Locate and identify every blood parasite.
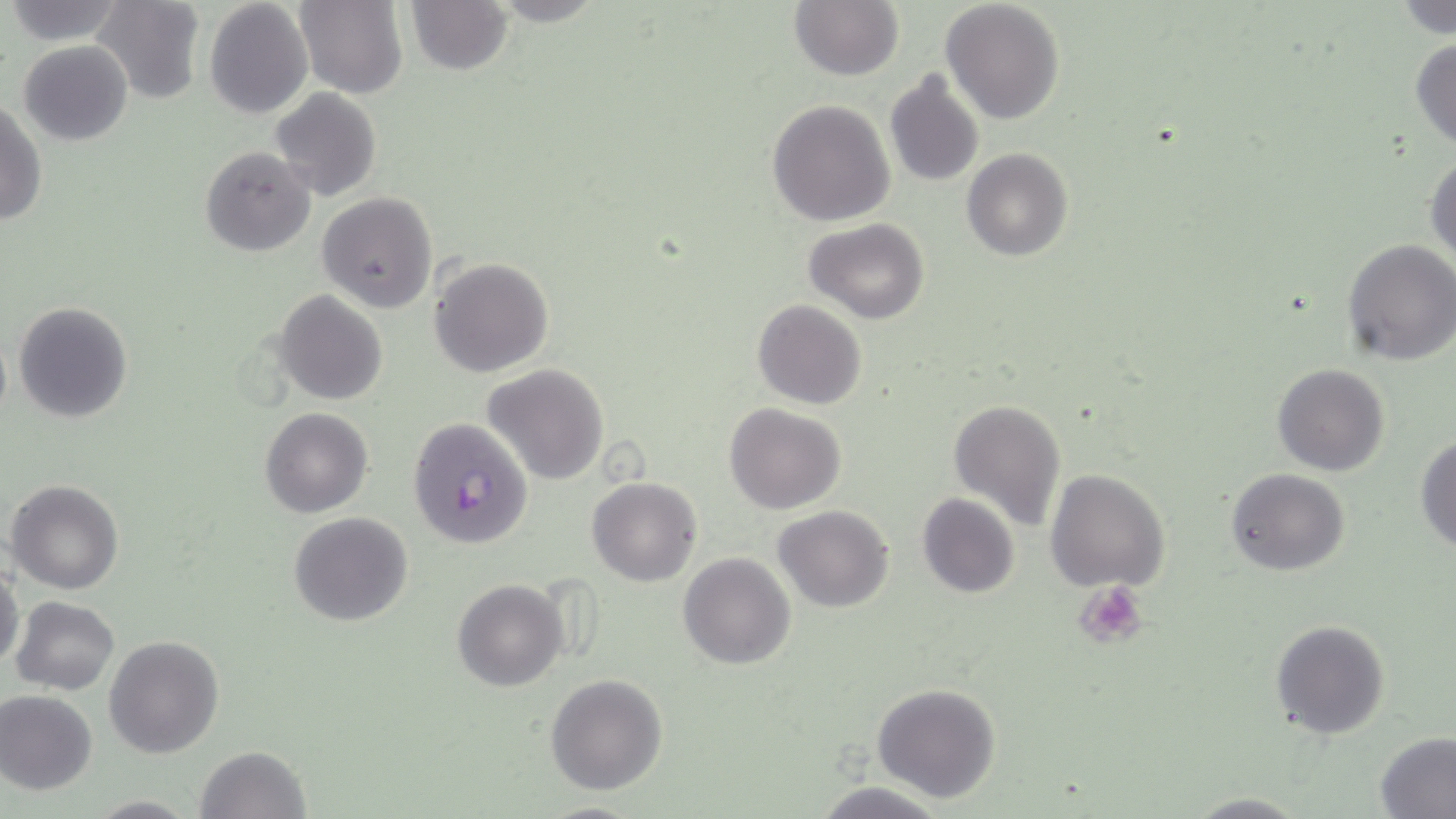
Approximate bounding boxes as named x1/y1/x2/y2 corners in pixels.
Plasmodium falciparum-infected red blood cells: (x1=406, y1=418, x2=533, y2=551).
No Plasmodium ovale, Plasmodium malariae, Plasmodium vivax, Babesia divergens, or Trypanosoma brucei observed.

Summary:
  - Platelet locations: (x1=1072, y1=581, x2=1147, y2=649)
  - Uninfected red blood cell locations: (x1=91, y1=0, x2=206, y2=104), (x1=205, y1=0, x2=313, y2=120), (x1=404, y1=0, x2=514, y2=75), (x1=3, y1=1, x2=127, y2=46), (x1=294, y1=1, x2=407, y2=97), (x1=789, y1=1, x2=904, y2=80), (x1=940, y1=1, x2=1066, y2=125), (x1=1394, y1=2, x2=1455, y2=39), (x1=1409, y1=35, x2=1456, y2=151), (x1=18, y1=40, x2=133, y2=147), (x1=883, y1=68, x2=984, y2=188), (x1=268, y1=87, x2=381, y2=203), (x1=0, y1=99, x2=47, y2=228), (x1=767, y1=99, x2=896, y2=227), (x1=201, y1=144, x2=316, y2=258), (x1=961, y1=148, x2=1072, y2=262), (x1=1425, y1=150, x2=1456, y2=267), (x1=318, y1=192, x2=436, y2=312), (x1=803, y1=217, x2=931, y2=324), (x1=1342, y1=238, x2=1456, y2=366), (x1=429, y1=257, x2=551, y2=377), (x1=276, y1=291, x2=387, y2=406), (x1=753, y1=299, x2=867, y2=410), (x1=13, y1=301, x2=133, y2=423), (x1=0, y1=324, x2=11, y2=434), (x1=482, y1=363, x2=610, y2=486), (x1=1272, y1=364, x2=1391, y2=477), (x1=947, y1=398, x2=1067, y2=531), (x1=724, y1=403, x2=848, y2=514), (x1=260, y1=407, x2=372, y2=518), (x1=1414, y1=432, x2=1456, y2=554), (x1=1045, y1=468, x2=1169, y2=592), (x1=1226, y1=468, x2=1350, y2=578), (x1=587, y1=475, x2=702, y2=586), (x1=7, y1=479, x2=124, y2=595), (x1=916, y1=492, x2=1021, y2=598), (x1=773, y1=504, x2=895, y2=613), (x1=289, y1=512, x2=414, y2=626), (x1=679, y1=553, x2=796, y2=671), (x1=0, y1=562, x2=24, y2=670), (x1=453, y1=578, x2=569, y2=692), (x1=11, y1=596, x2=120, y2=694), (x1=1270, y1=618, x2=1391, y2=740), (x1=104, y1=636, x2=226, y2=758), (x1=545, y1=674, x2=668, y2=795), (x1=871, y1=683, x2=1002, y2=803), (x1=0, y1=690, x2=99, y2=796), (x1=1374, y1=733, x2=1456, y2=818), (x1=194, y1=746, x2=310, y2=819), (x1=810, y1=779, x2=955, y2=819), (x1=1183, y1=791, x2=1311, y2=817), (x1=83, y1=795, x2=200, y2=817), (x1=534, y1=800, x2=649, y2=818)
  - Slide-level diagnosis: Plasmodium falciparum
  - Modality: optical microscopy
  - Image size: 1456×819 pixels
  - Magnification: 1000x
  - Preparation: thin blood film
  - Stain: May-Grünwald-Giemsa
  - Field of view: single